Assess for parasitized red blood cells.
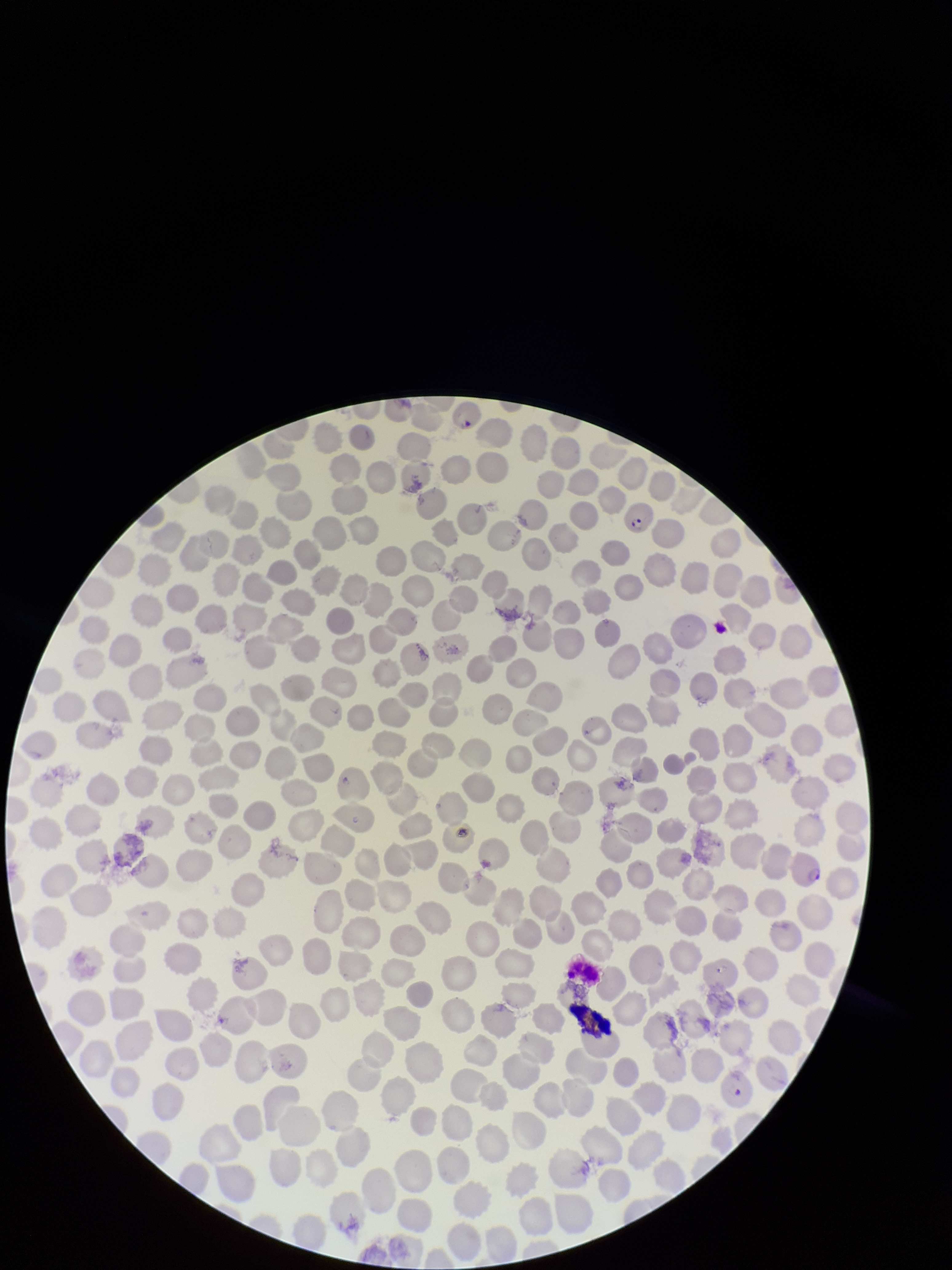
Seen.

Summary:
  - Stain: Giemsa
  - Image size: 952×1270 pixels
  - Red blood cell count: 295
  - Capture: smartphone photograph through the microscope eyepiece
  - Field of view: one from this slide
  - Parasitized red blood cell count: 3
  - Species reported for this patient: Plasmodium falciparum
  - Patient malaria status: infected
  - Preparation: thin blood smear